Outline each Plasmodium malariae-infected red blood cell.
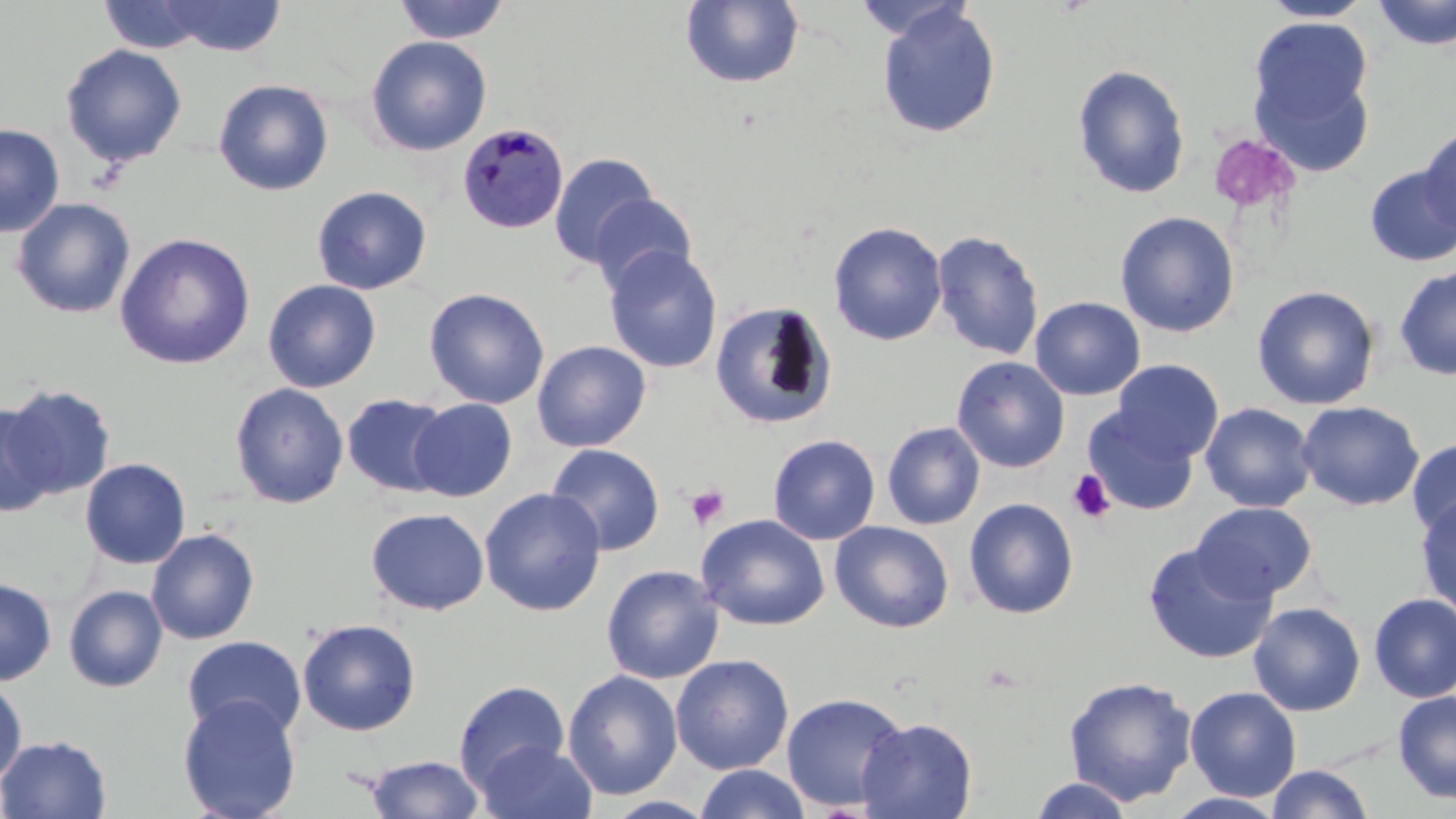
Approximate bounding boxes as named x1/y1/x2/y2 corners in pixels.
Plasmodium malariae-infected red blood cells: (x1=457, y1=121, x2=569, y2=234).

slide-level diagnosis = Plasmodium malariae
stain = May-Grünwald-Giemsa
platelet locations = approximate bounding boxes as named x1/y1/x2/y2 corners in pixels: (x1=1207, y1=132, x2=1299, y2=215), (x1=1067, y1=469, x2=1117, y2=523), (x1=686, y1=485, x2=729, y2=530)
uninfected red blood cell locations = approximate bounding boxes as named x1/y1/x2/y2 corners in pixels: (x1=97, y1=0, x2=215, y2=54), (x1=156, y1=0, x2=287, y2=57), (x1=393, y1=0, x2=510, y2=44), (x1=1372, y1=0, x2=1456, y2=50), (x1=680, y1=1, x2=804, y2=89), (x1=1260, y1=1, x2=1373, y2=23), (x1=876, y1=4, x2=1001, y2=139), (x1=1247, y1=17, x2=1375, y2=158), (x1=365, y1=35, x2=492, y2=156), (x1=60, y1=43, x2=188, y2=168), (x1=1072, y1=63, x2=1191, y2=200), (x1=213, y1=78, x2=334, y2=196), (x1=0, y1=123, x2=64, y2=238), (x1=1418, y1=125, x2=1456, y2=237), (x1=549, y1=151, x2=659, y2=268), (x1=1363, y1=164, x2=1456, y2=267), (x1=311, y1=185, x2=432, y2=295), (x1=589, y1=193, x2=698, y2=294), (x1=12, y1=197, x2=136, y2=318), (x1=1115, y1=210, x2=1240, y2=338), (x1=827, y1=221, x2=948, y2=346), (x1=930, y1=229, x2=1044, y2=361), (x1=114, y1=232, x2=256, y2=369), (x1=603, y1=246, x2=723, y2=374), (x1=1394, y1=267, x2=1456, y2=380), (x1=262, y1=279, x2=381, y2=393), (x1=1252, y1=285, x2=1380, y2=410), (x1=423, y1=287, x2=549, y2=409), (x1=1029, y1=296, x2=1145, y2=401), (x1=708, y1=300, x2=837, y2=430), (x1=532, y1=340, x2=652, y2=452), (x1=951, y1=355, x2=1070, y2=473), (x1=1111, y1=359, x2=1223, y2=464), (x1=229, y1=382, x2=349, y2=509), (x1=3, y1=384, x2=116, y2=500), (x1=341, y1=393, x2=452, y2=497), (x1=408, y1=398, x2=517, y2=501), (x1=1296, y1=400, x2=1425, y2=511), (x1=1200, y1=402, x2=1318, y2=512), (x1=0, y1=403, x2=59, y2=517), (x1=1082, y1=406, x2=1199, y2=516), (x1=882, y1=421, x2=985, y2=530), (x1=767, y1=433, x2=880, y2=545), (x1=1407, y1=438, x2=1456, y2=542), (x1=547, y1=443, x2=665, y2=556), (x1=79, y1=458, x2=191, y2=570), (x1=479, y1=487, x2=606, y2=616), (x1=1415, y1=496, x2=1456, y2=618), (x1=964, y1=497, x2=1079, y2=619), (x1=1191, y1=501, x2=1317, y2=602), (x1=366, y1=508, x2=489, y2=616), (x1=696, y1=514, x2=830, y2=631), (x1=830, y1=520, x2=954, y2=633), (x1=146, y1=528, x2=260, y2=645), (x1=1142, y1=543, x2=1276, y2=664), (x1=601, y1=564, x2=724, y2=685), (x1=0, y1=577, x2=57, y2=686), (x1=63, y1=585, x2=168, y2=693), (x1=1369, y1=592, x2=1456, y2=702), (x1=1248, y1=602, x2=1365, y2=716), (x1=297, y1=619, x2=421, y2=736), (x1=181, y1=635, x2=306, y2=740), (x1=670, y1=654, x2=793, y2=775), (x1=562, y1=670, x2=683, y2=801), (x1=1062, y1=675, x2=1198, y2=807), (x1=0, y1=679, x2=27, y2=786), (x1=453, y1=680, x2=570, y2=794), (x1=1184, y1=685, x2=1302, y2=801), (x1=1393, y1=691, x2=1456, y2=804), (x1=781, y1=692, x2=909, y2=813), (x1=178, y1=695, x2=302, y2=819), (x1=857, y1=716, x2=978, y2=818), (x1=0, y1=734, x2=112, y2=818), (x1=475, y1=741, x2=598, y2=819), (x1=364, y1=755, x2=484, y2=818), (x1=694, y1=764, x2=812, y2=819), (x1=1266, y1=764, x2=1374, y2=819), (x1=1029, y1=777, x2=1134, y2=818), (x1=1165, y1=791, x2=1290, y2=818), (x1=603, y1=795, x2=718, y2=819)
image size = 1456×819 pixels
field of view = single
preparation = thin blood smear
magnification = 1000x
modality = optical microscopy